Classify this cell by malaria status.
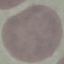

It is uninfected.

Thin blood film. Giemsa stain. Photographed with a smartphone camera at the microscope eyepiece. Automatically extracted cell patch, resized to 64 × 64 pixels.